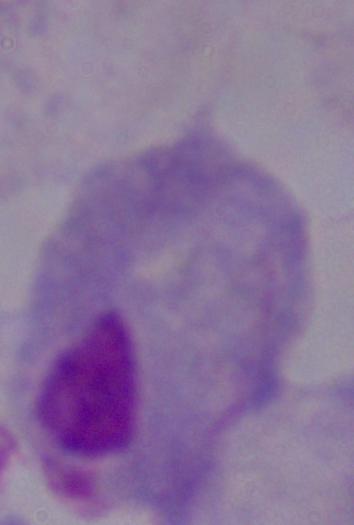
{
  "magnification": "1000x",
  "modality": "photomicrograph",
  "identification": "trichomonad"
}